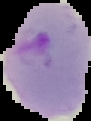

From a thin blood film. Image is 91×121 pixels. Result: Plasmodium parasites identified. Cell region segmented out of the field of view; the surrounding area is masked to black.